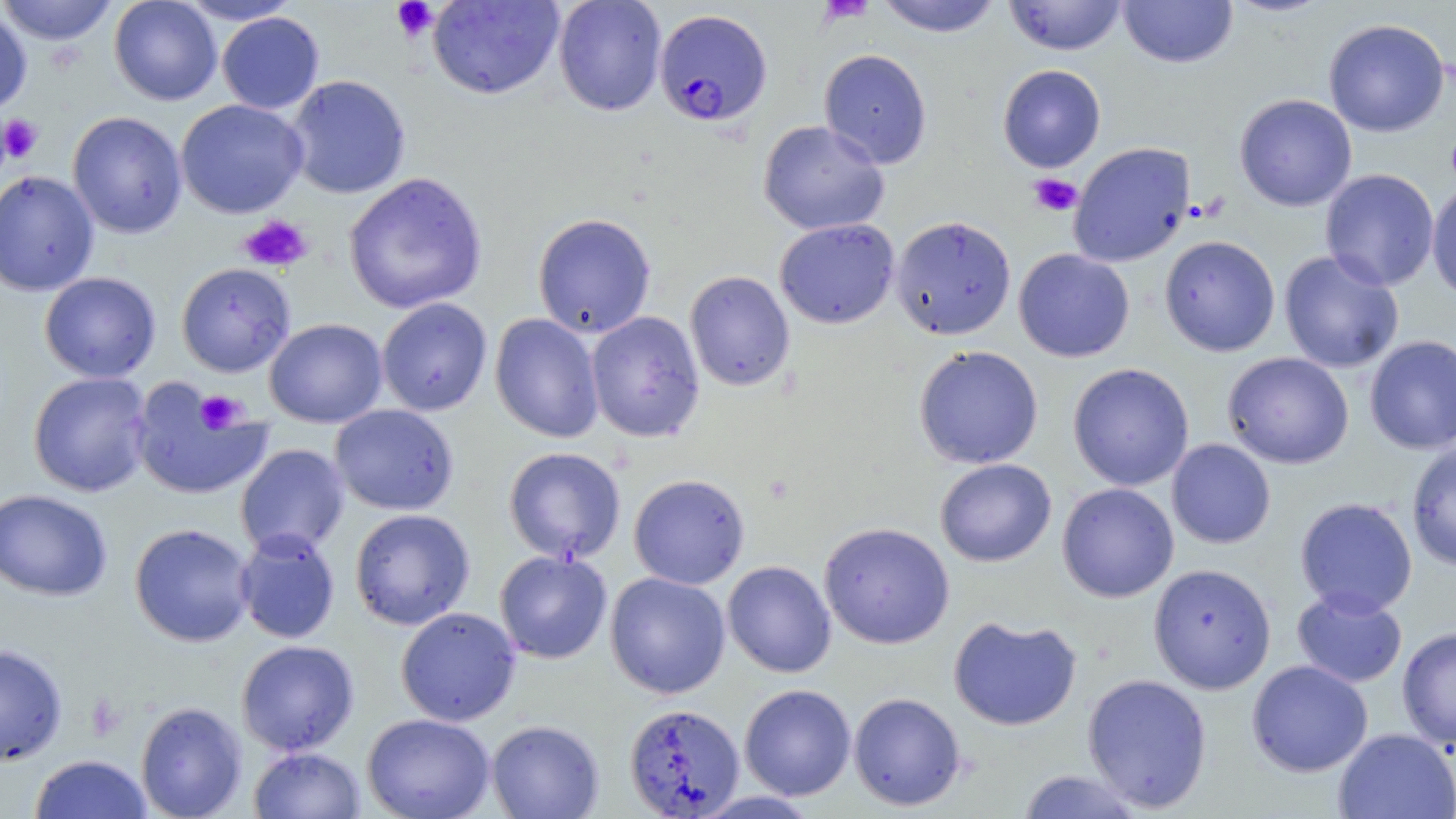

Approximate bounding boxes as (x1,y1)-(x2,y2) corner pairs in pixels. Uninfected red blood cell locations: (0,0)-(118,45), (109,0)-(222,106), (177,0)-(303,24), (553,0)-(667,116), (874,0)-(1003,37), (1003,0)-(1127,56), (1118,0)-(1237,68), (1222,0)-(1334,18), (427,1)-(564,100), (0,6)-(32,116), (217,12)-(324,114), (1323,18)-(1450,138), (819,48)-(932,169), (997,64)-(1106,173), (286,74)-(411,199), (1234,93)-(1357,212), (175,99)-(308,218), (67,111)-(187,238), (758,119)-(890,235), (1068,141)-(1195,268), (1319,168)-(1439,291), (0,169)-(99,296), (343,171)-(488,315), (1427,183)-(1456,303), (532,213)-(656,338), (890,215)-(1017,340), (774,218)-(900,329), (1159,235)-(1281,357), (1013,248)-(1135,362), (1278,250)-(1404,373), (176,262)-(296,377), (684,270)-(795,391), (39,271)-(161,383), (376,298)-(493,416), (586,311)-(705,442), (490,313)-(604,443), (265,318)-(387,427), (1364,335)-(1456,455), (913,345)-(1044,469), (1222,352)-(1354,469), (1067,363)-(1194,491), (28,372)-(152,497), (129,380)-(272,500), (329,404)-(459,515), (1166,439)-(1276,548), (1406,441)-(1456,571), (235,444)-(350,557), (504,446)-(626,564), (935,458)-(1057,567), (629,473)-(750,589), (1057,483)-(1179,602), (0,488)-(113,601), (1295,497)-(1417,617), (349,508)-(475,630), (818,521)-(955,649), (130,523)-(255,647), (234,529)-(340,644), (495,550)-(612,664), (722,560)-(837,678), (1149,563)-(1276,693), (605,571)-(731,699), (1291,589)-(1408,688), (395,607)-(521,726), (948,615)-(1082,731), (1397,627)-(1456,750), (236,640)-(359,756), (0,643)-(68,765), (1246,660)-(1373,777), (1082,673)-(1213,812), (739,684)-(856,800), (848,692)-(966,811), (135,701)-(248,818), (624,703)-(745,817), (361,713)-(496,819), (486,719)-(604,819), (1333,728)-(1456,819), (249,746)-(365,818), (30,754)-(152,818), (1016,768)-(1147,818), (690,790)-(825,818). Plasmodium falciparum-infected red blood cell locations: (655,9)-(772,127). Platelet locations: (816,0)-(875,23), (391,1)-(437,42), (0,114)-(43,163), (1028,173)-(1082,217), (238,215)-(313,272), (195,390)-(246,433). Slide-level diagnosis: Plasmodium falciparum. Thin blood smear. May-Grünwald-Giemsa stain. Image is 1456×819 pixels. Single field of view. Captured at 1000x magnification. Optical microscopy.